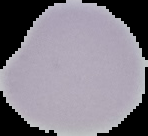

{
  "image_size": "148×136 pixels",
  "image_type": "segmented cell region on a black background",
  "preparation": "thin blood smear",
  "malaria_status": "uninfected"
}